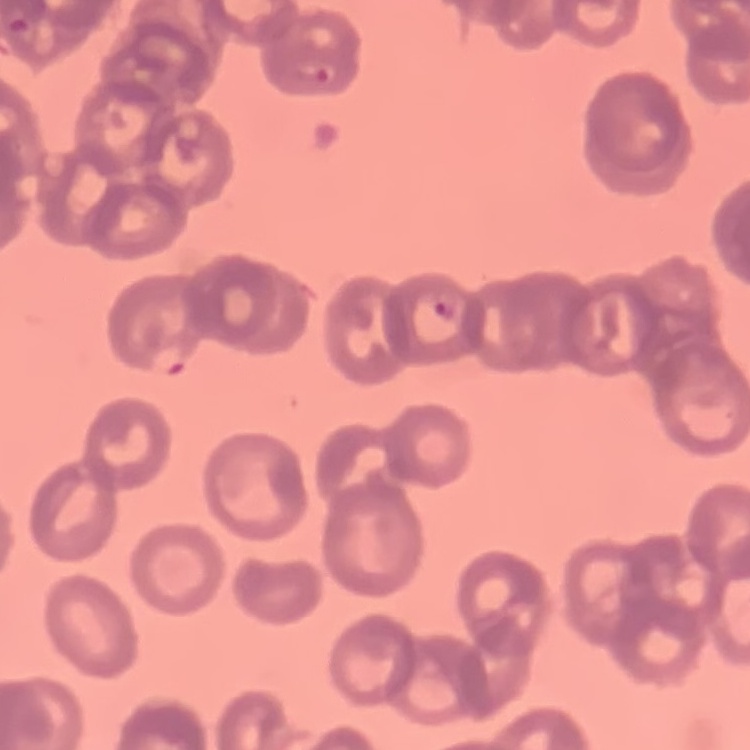

Summary:
  - Erythrocyte morphology: rouleaux formation
  - Stain: Field's or Giemsa
  - Image type: one tile cut from a larger photomicrograph
  - Preparation: thin blood film